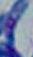

modality: micrograph
magnification: 1000x
identification: Toxoplasma gondii